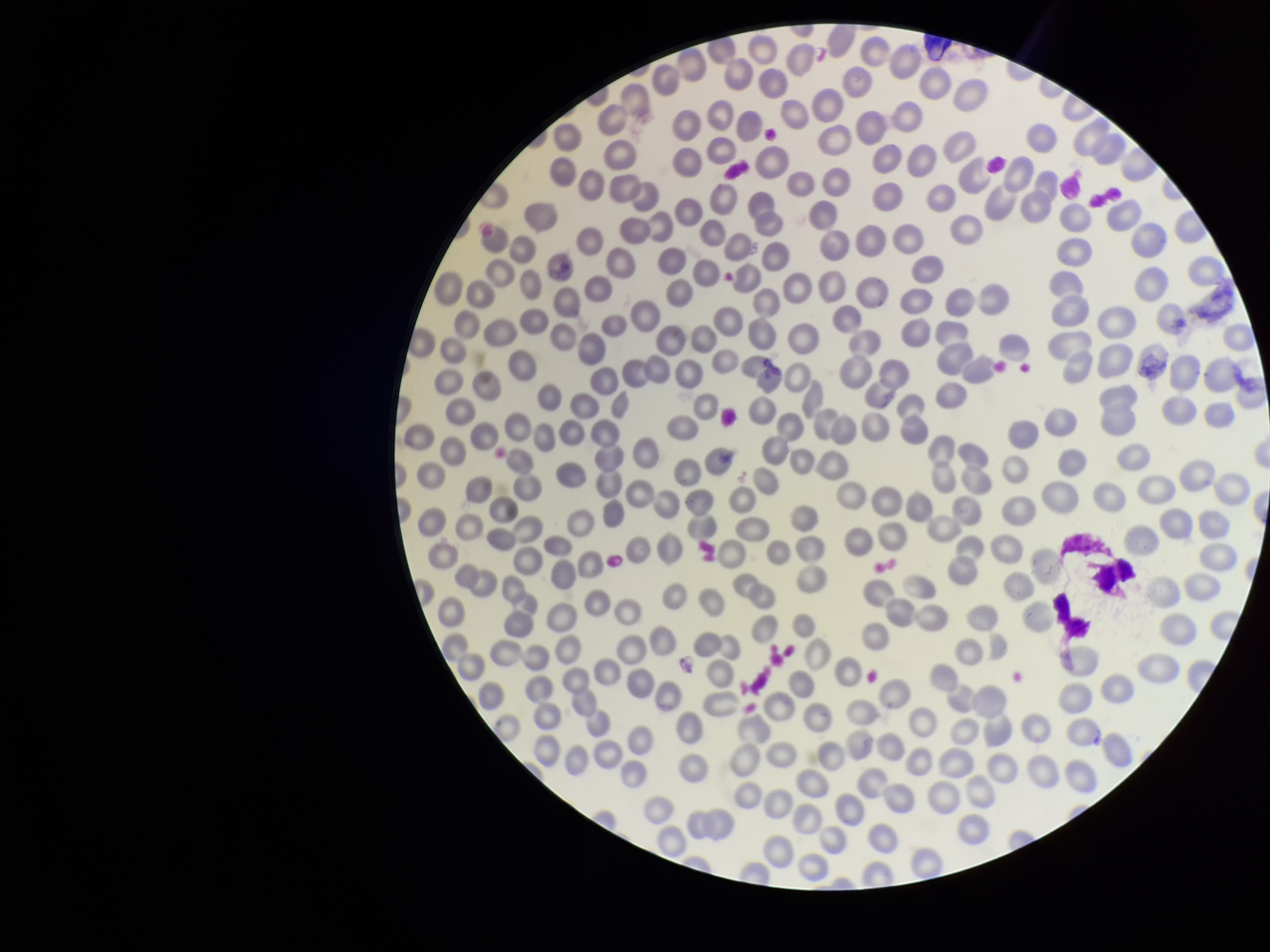

Summary:
  - Image size: 1270×952 pixels
  - Patient malaria status: negative
  - Capture: smartphone photograph through the microscope eyepiece
  - Parasitized red blood cell count: 0
  - Field of view: single
  - Stain: Giemsa
  - Preparation: thin blood smear
  - Parasitized red blood cells: none detected
  - Red blood cell count: 269